Report the malaria status of this cell.
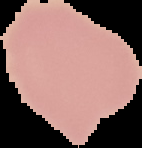

Uninfected.

Image is 142×148 pixels. From a thin blood smear. The area outside the segmented cell region is set to black.